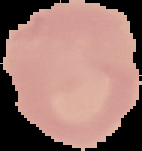

Image is 142×151 pixels. Malaria status: uninfected. Segmented cell region on a black background. From a thin blood film.